State which parasite is depicted.
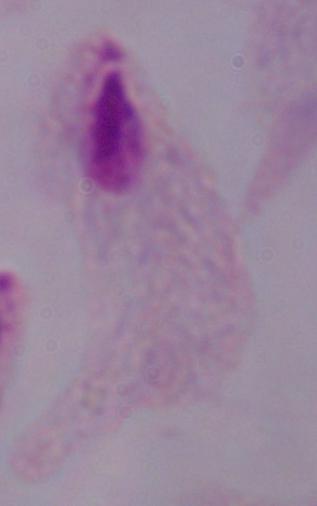
This is a trichomonad.

Photomicrograph. 1000x magnification.